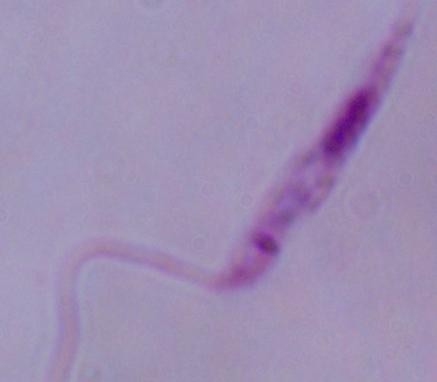
magnification: 1000x
identification: Leishmania
modality: micrograph